Classify this cell by malaria status.
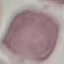
Uninfected.

Giemsa-stained preparation. Cell patch, automatically extracted from a larger field of view and resized to 64 × 64 pixels. Thin blood smear. Photographed with a smartphone camera at the microscope eyepiece.